Name the parasite shown.
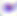
Toxoplasma gondii.

Summary:
  - Modality: photomicrograph
  - Magnification: 400x